Classify this cell by malaria status.
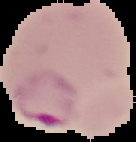
Parasitized.

Summary:
  - Preparation: thin blood film
  - Image size: 136×142 pixels
  - Image type: cell region segmented out of the field of view; surrounding area masked to black